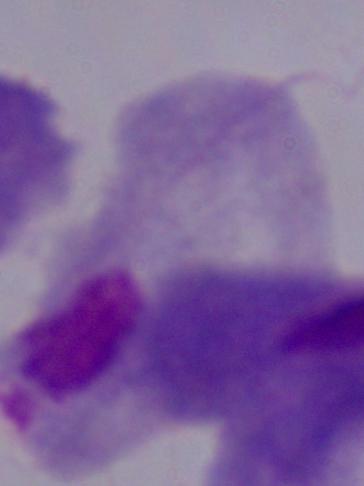
Summary:
  - Magnification: 1000x
  - Identification: trichomonad
  - Modality: micrograph